Report the malaria status of this cell.
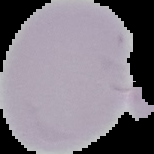
It is uninfected.

Summary:
  - Image size: 154×154 pixels
  - Image type: segmented cell region on a black background
  - Preparation: thin blood film